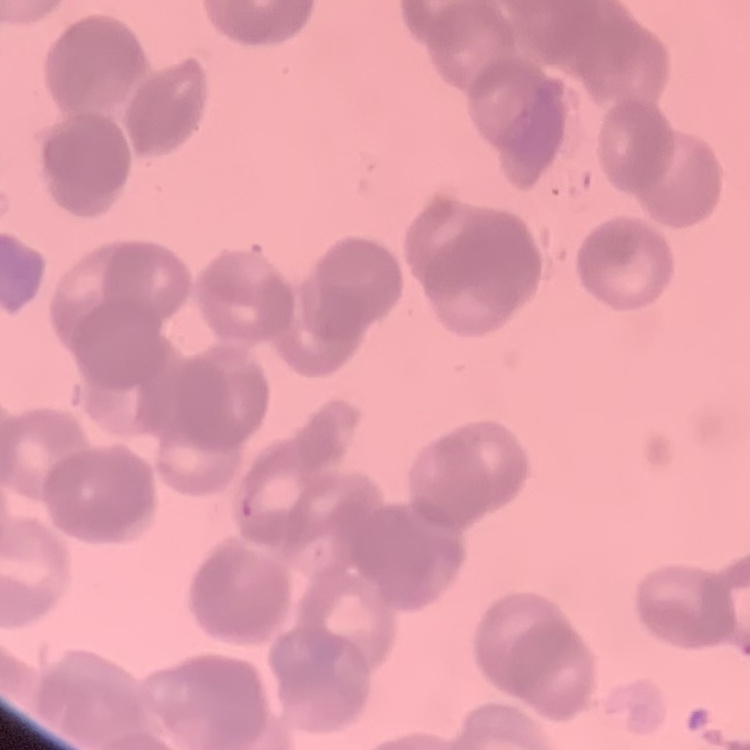
Summary:
  - Erythrocyte morphology: rouleaux formation
  - Image type: one tile cut from a larger photomicrograph
  - Stain: Field's or Giemsa
  - Preparation: thin blood smear